Locate and identify every blood parasite.
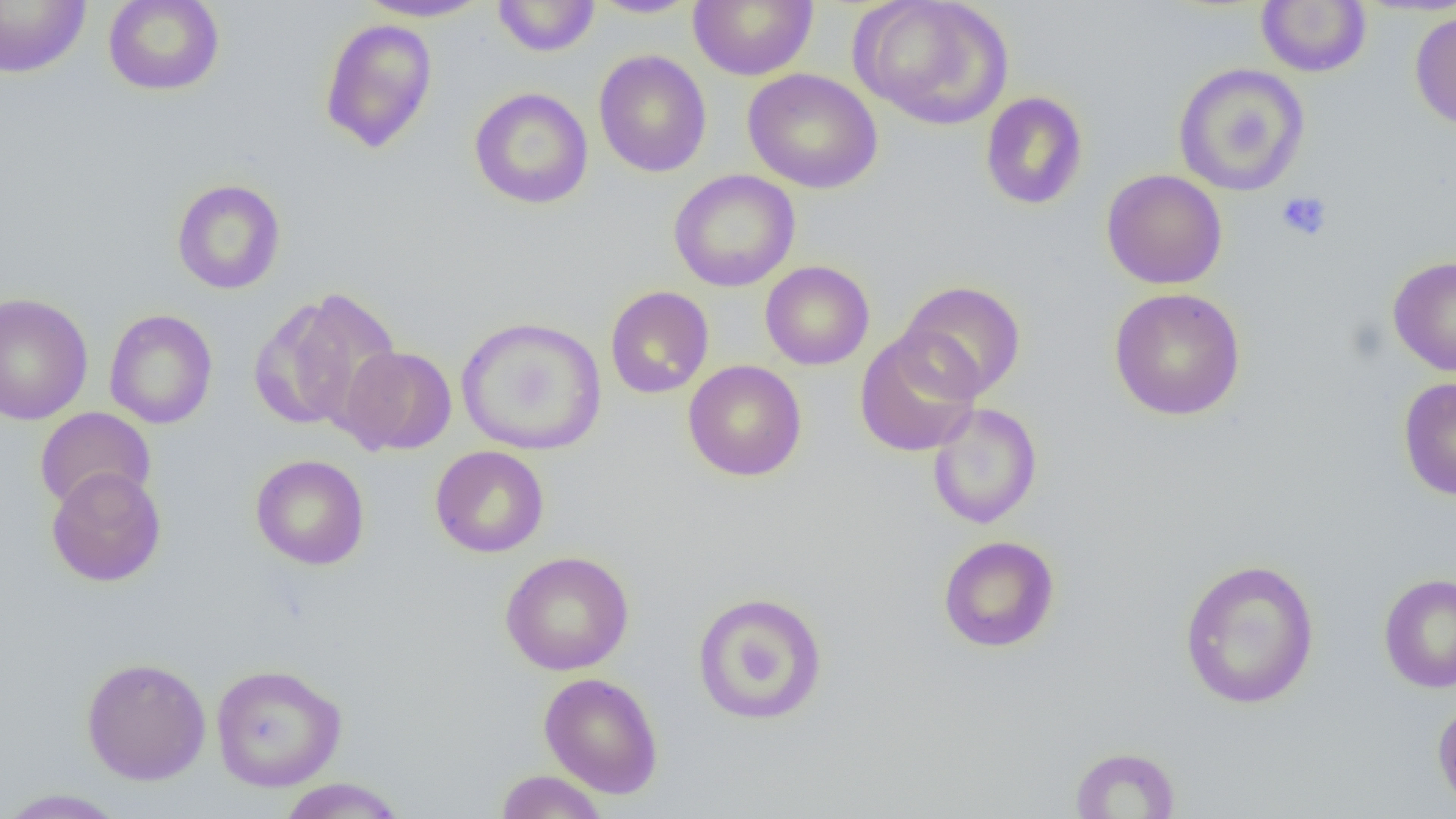

No blood parasites observed.

slide-level diagnosis = negative for blood parasites
preparation = thin blood film
platelet locations = approximate bounding boxes as [x1, y1, x2, y2] in pixels: [1276, 191, 1332, 242]
uninfected red blood cell locations = approximate bounding boxes as [x1, y1, x2, y2] in pixels: [103, 0, 225, 96], [355, 0, 493, 22], [492, 0, 600, 57], [588, 0, 700, 19], [689, 0, 817, 81], [852, 0, 1014, 130], [0, 1, 91, 78], [1256, 1, 1372, 77], [1409, 8, 1456, 131], [319, 18, 438, 153], [593, 50, 712, 178], [1173, 63, 1310, 197], [743, 68, 883, 194], [469, 87, 594, 210], [980, 91, 1089, 210], [669, 169, 801, 292], [1101, 169, 1228, 289], [171, 178, 286, 295], [1388, 256, 1456, 377], [760, 260, 875, 370], [898, 280, 1027, 402], [604, 286, 714, 399], [1108, 287, 1246, 421], [253, 288, 403, 432], [0, 292, 94, 425], [104, 309, 218, 429], [456, 316, 607, 455], [854, 330, 981, 457], [338, 345, 457, 455], [683, 360, 807, 481], [1398, 376, 1456, 501], [927, 402, 1042, 529], [34, 407, 156, 512], [430, 445, 549, 558], [250, 454, 370, 570], [46, 467, 166, 587], [938, 535, 1060, 652], [500, 550, 635, 676], [1179, 558, 1320, 709], [1378, 572, 1456, 693], [692, 591, 829, 726], [81, 656, 211, 785], [210, 663, 347, 792], [539, 672, 664, 799], [1432, 698, 1456, 814], [1069, 746, 1181, 818], [495, 769, 609, 818], [275, 778, 410, 818], [0, 788, 129, 818]
field of view = one of a larger specimen
image size = 1456×819 pixels
magnification = 1000x
modality = optical microscopy